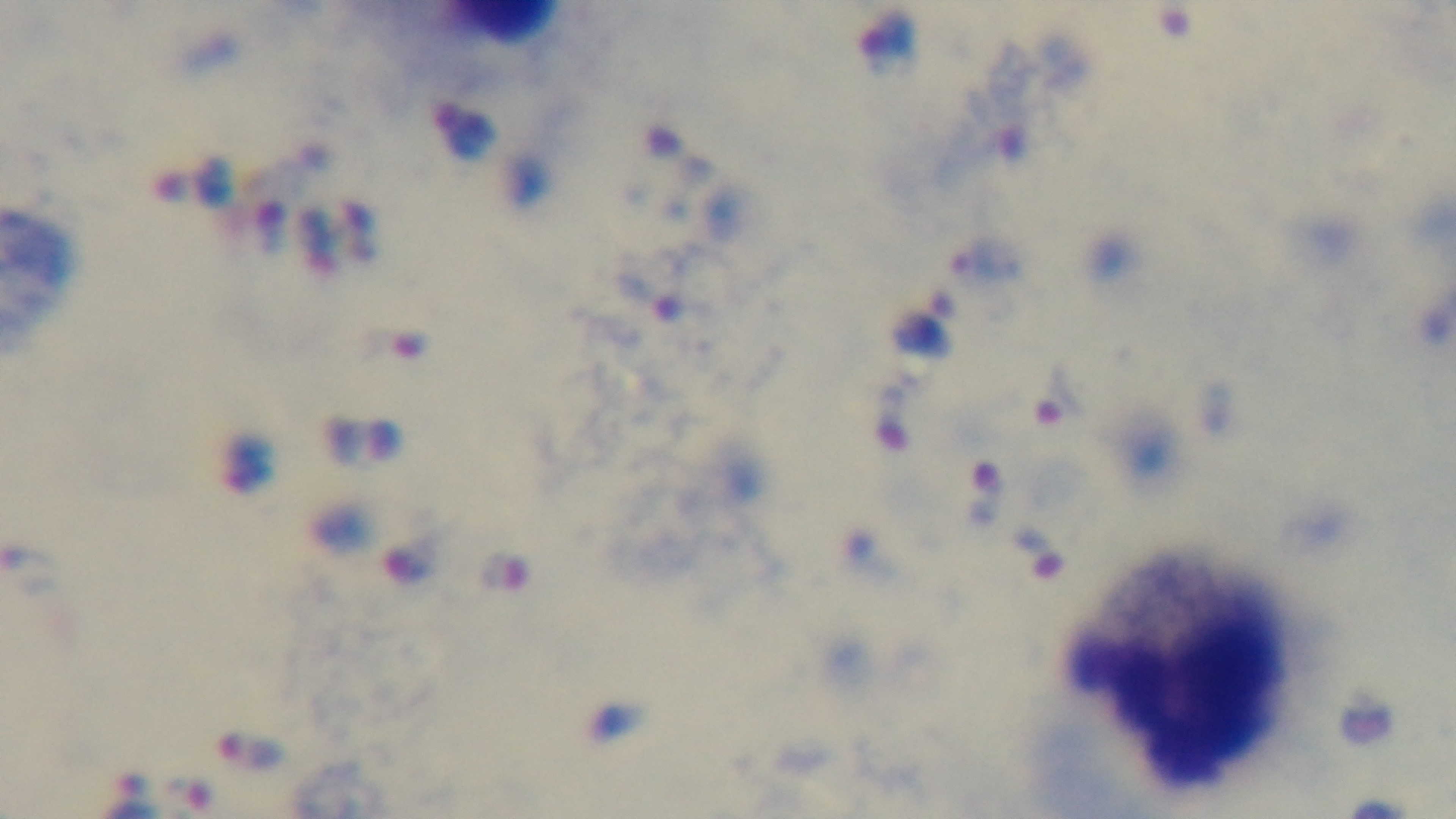 Giemsa stain. Oil-immersion objective, 100x. Captured with a mounted 4K digital camera. Light microscopy. Preparation: thick. Malaria status: positive. One field from the slide.